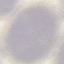
result = negative for malaria parasites
stain = Giemsa
image type = cell patch, automatically extracted from a larger field of view and resized to 64 × 64 pixels
capture = smartphone through the microscope eyepiece
preparation = thin blood film